Report the malaria status of this cell.
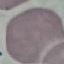
Uninfected.

{
  "capture": "smartphone camera at the microscope eyepiece",
  "preparation": "thin blood film",
  "stain": "Giemsa",
  "image_type": "automatically extracted cell patch, resized to 64 × 64 pixels"
}